Describe the morphology of the erythrocytes.
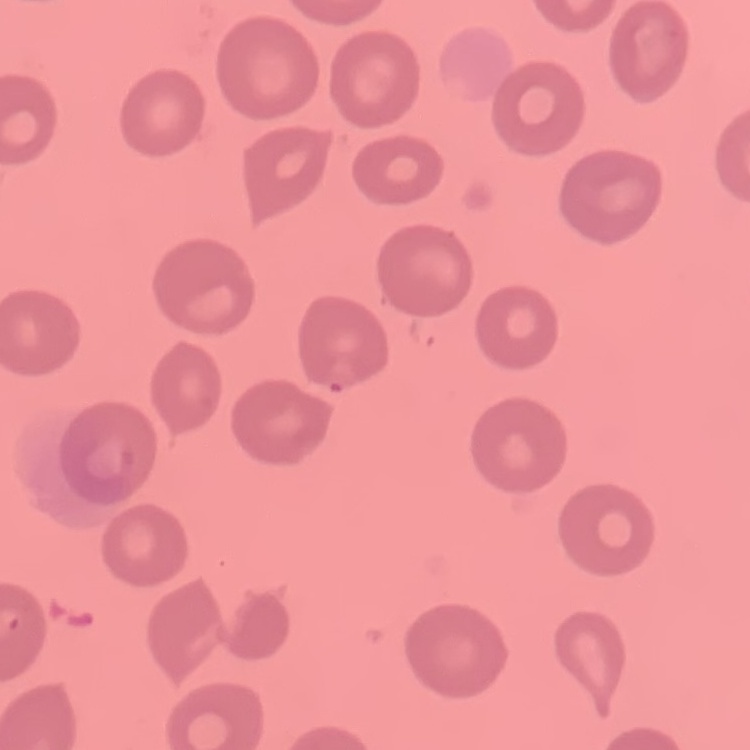

No rouleaux formation.

image_type: square crop of a larger photomicrograph
preparation: thin blood smear
stain: Field's or Giemsa